Give the position of every leukocyte visible.
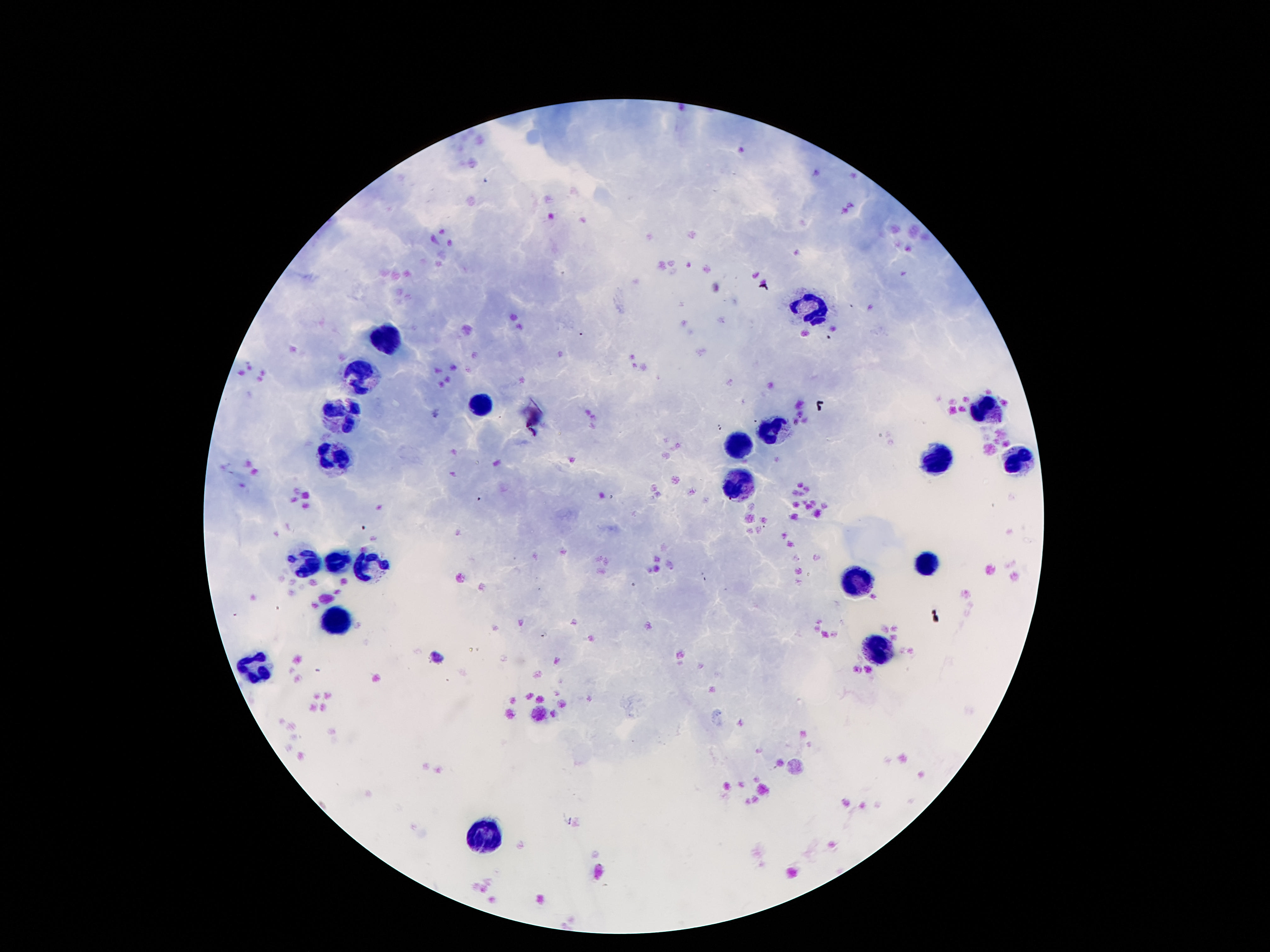

Approximate centers as (x, y) in pixels.
Leukocytes: (814, 306), (388, 335), (362, 374), (481, 407), (990, 408), (345, 419), (781, 427), (736, 443), (337, 458), (939, 462), (1017, 464), (732, 486), (304, 562), (337, 562), (925, 562), (368, 566), (861, 585), (339, 621), (876, 653), (257, 671), (478, 836).

Summary:
  - Preparation: thick peripheral-blood smear
  - Patient malaria status: negative
  - Stain: Giemsa
  - Image size: 1270×952 pixels
  - Capture: smartphone camera through the microscope eyepiece
  - Magnification: 100x
  - Field of view: one from this slide